Give the extent of all Plasmodium falciparum-infected red blood cells.
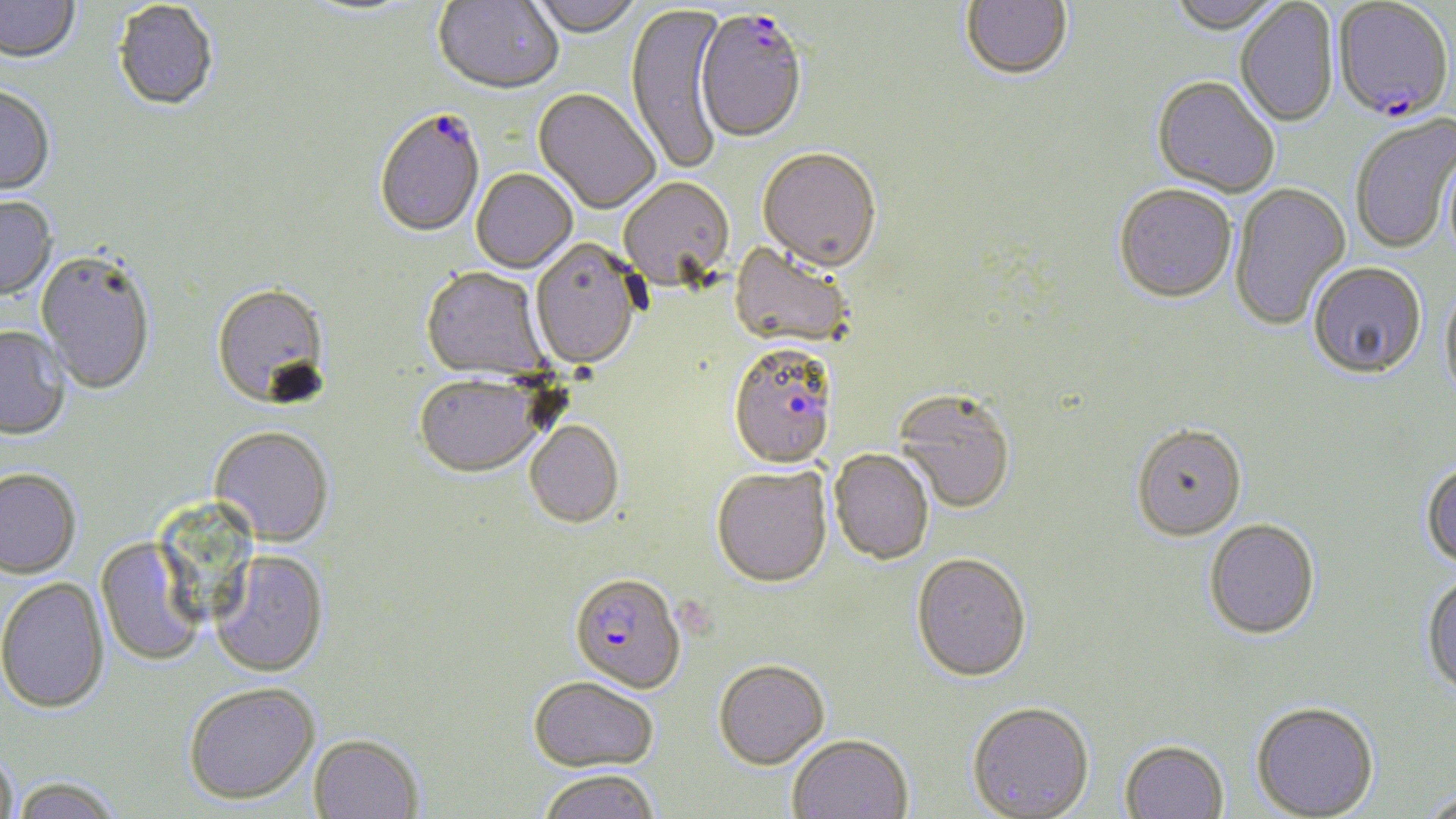

Approximate bounding boxes as (x1, y1, x2, y2) in pixels.
Plasmodium falciparum-infected red blood cells: (1333, 1, 1454, 124), (694, 14, 807, 146), (374, 111, 485, 240), (731, 347, 841, 474), (570, 576, 686, 696).

slide-level diagnosis = Plasmodium falciparum
modality = light microscopy
stain = May-Grünwald-Giemsa
preparation = thin blood film
magnification = 1000x
field of view = one of a larger specimen
image size = 1456×819 pixels
uninfected red blood cell locations = approximate bounding boxes as (x1, y1, x2, y2) in pixels: (433, 0, 563, 97), (527, 0, 642, 40), (961, 0, 1073, 84), (1167, 0, 1284, 36), (0, 1, 80, 67), (297, 1, 423, 20), (1235, 1, 1339, 129), (113, 3, 218, 114), (625, 3, 728, 177), (1151, 79, 1279, 199), (0, 88, 56, 199), (532, 90, 658, 215), (1350, 115, 1456, 254), (758, 151, 881, 275), (471, 170, 577, 273), (619, 179, 735, 295), (1229, 183, 1351, 332), (1114, 187, 1237, 306), (0, 197, 57, 302), (529, 241, 642, 372), (727, 243, 852, 353), (34, 252, 156, 396), (1309, 262, 1428, 380), (420, 269, 549, 384), (1440, 281, 1456, 408), (211, 285, 332, 412), (0, 328, 70, 442), (413, 378, 544, 480), (894, 391, 1016, 516), (524, 423, 624, 530), (1131, 427, 1246, 544), (208, 428, 334, 547), (829, 451, 934, 567), (1421, 460, 1456, 571), (711, 468, 832, 591), (0, 471, 81, 581), (1204, 519, 1321, 641), (95, 539, 204, 666), (209, 552, 329, 679), (911, 556, 1032, 686), (1421, 571, 1456, 702), (0, 579, 110, 717), (713, 663, 829, 773), (527, 679, 659, 776), (184, 685, 320, 809), (1250, 702, 1379, 819), (966, 705, 1095, 819), (307, 736, 424, 819), (788, 737, 913, 819), (1119, 742, 1228, 819), (0, 748, 19, 819), (538, 772, 660, 819), (11, 779, 121, 819), (1415, 788, 1456, 818)